Report the malaria status of this cell.
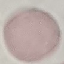

Uninfected.

{
  "capture": "smartphone camera at the microscope eyepiece",
  "stain": "Giemsa",
  "image_type": "cell patch, automatically extracted from a larger field of view and resized to 64 × 64 pixels",
  "preparation": "thin smear"
}